Identify the blood parasite species.
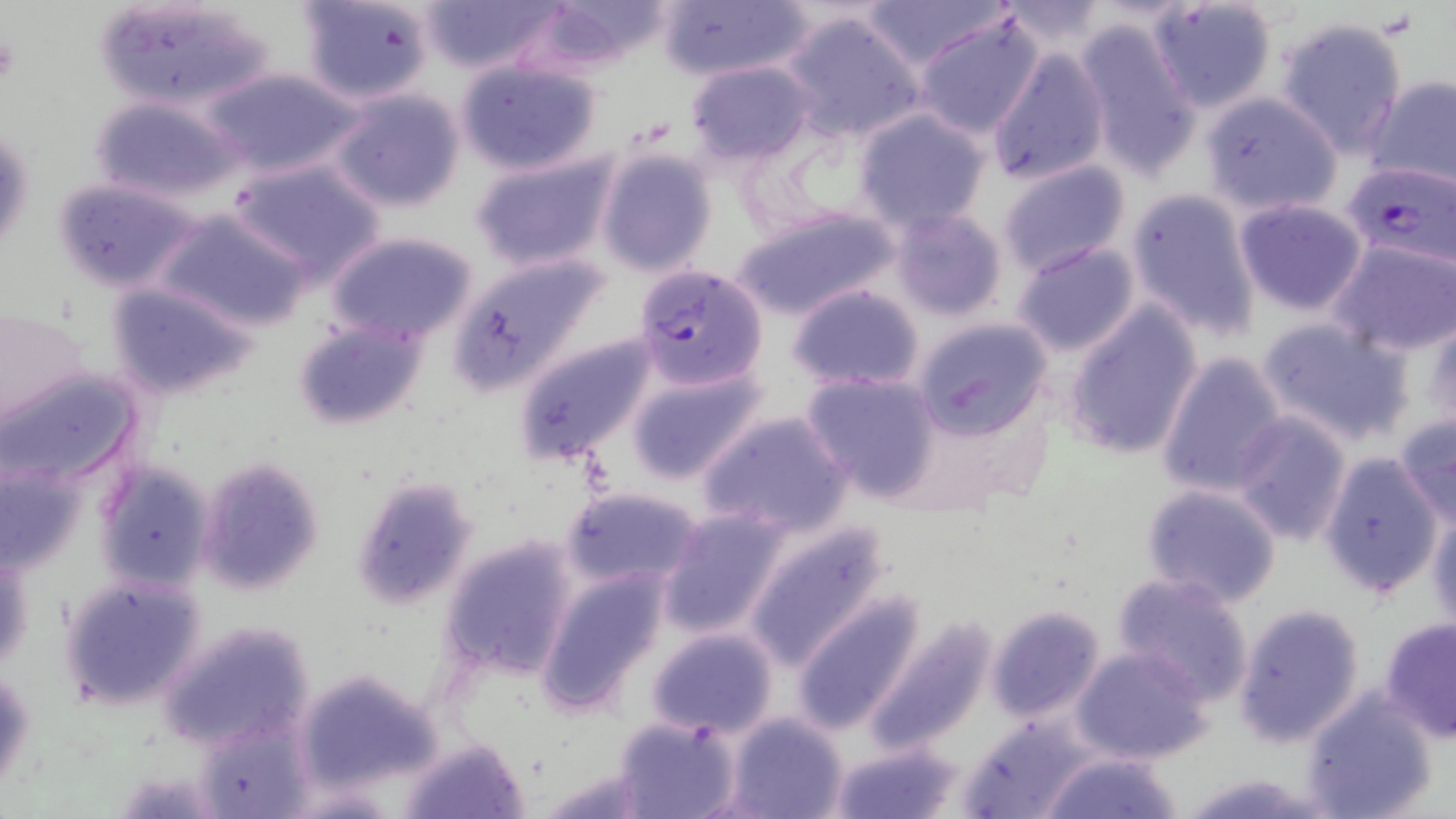
Plasmodium falciparum.

modality = optical microscopy
uninfected red blood cell locations = approximate bounding boxes as (x1,y1)-(x2,y2) corner pairs in pixels: (298,0)-(437,104), (420,0)-(562,74), (654,0)-(812,82), (852,0)-(1012,70), (91,1)-(276,113), (523,2)-(673,74), (997,2)-(1115,55), (1147,2)-(1279,113), (781,11)-(928,144), (914,14)-(1043,139), (1274,16)-(1410,156), (1074,18)-(1201,177), (987,49)-(1109,185), (454,60)-(602,176), (686,61)-(815,164), (203,68)-(360,179), (1362,75)-(1456,193), (327,86)-(468,213), (1197,88)-(1344,215), (90,96)-(242,202), (852,108)-(992,232), (1,115)-(34,263), (595,148)-(718,278), (470,149)-(620,274), (229,159)-(387,281), (996,161)-(1134,279), (52,178)-(202,293), (1124,188)-(1262,341), (1233,198)-(1368,317), (729,203)-(902,322), (155,208)-(316,334), (887,208)-(1007,321), (324,229)-(479,345), (1330,239)-(1456,357), (1011,241)-(1142,357), (449,253)-(610,397), (106,281)-(258,401), (787,284)-(924,390), (1061,301)-(1205,462), (0,306)-(91,436), (1256,316)-(1414,447), (293,317)-(430,431), (913,318)-(1053,438), (1423,318)-(1456,435), (513,328)-(663,465), (1155,351)-(1289,499), (623,360)-(768,485), (0,366)-(142,489), (801,371)-(942,502), (698,409)-(854,537), (1230,412)-(1353,546), (1394,413)-(1456,531), (1315,450)-(1447,600), (195,455)-(327,596), (0,460)-(87,579), (95,460)-(216,594), (350,475)-(478,611), (1141,483)-(1282,608), (562,486)-(703,592), (1427,503)-(1456,634), (657,506)-(794,640), (739,518)-(893,672), (440,534)-(580,680), (535,566)-(670,718), (1111,572)-(1255,706), (59,575)-(206,710), (791,593)-(926,735), (1231,602)-(1367,749), (985,604)-(1108,723), (864,615)-(999,753), (1379,616)-(1456,742), (160,618)-(316,753), (646,628)-(778,738), (1071,645)-(1214,765), (2,665)-(35,795), (294,667)-(445,791), (1300,691)-(1437,819), (726,712)-(849,819), (613,714)-(740,819), (960,716)-(1096,819), (399,736)-(528,818), (828,740)-(965,819), (1039,748)-(1184,819), (1175,772)-(1335,818)
magnification = 1000x
field of view = one of a larger specimen
image size = 1456×819 pixels
Plasmodium falciparum-infected red blood cell locations = approximate bounding boxes as (x1,y1)-(x2,y2) corner pairs in pixels: (1343,161)-(1456,272), (632,264)-(768,391)
preparation = thin blood smear
stain = May-Grünwald-Giemsa